Report the malaria status of this cell.
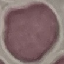

Uninfected.

image type = cell patch, automatically extracted from a larger field of view and resized to 64 × 64 pixels
capture = smartphone through the microscope eyepiece
stain = Giemsa
preparation = thin smear